Identify the preparation type.
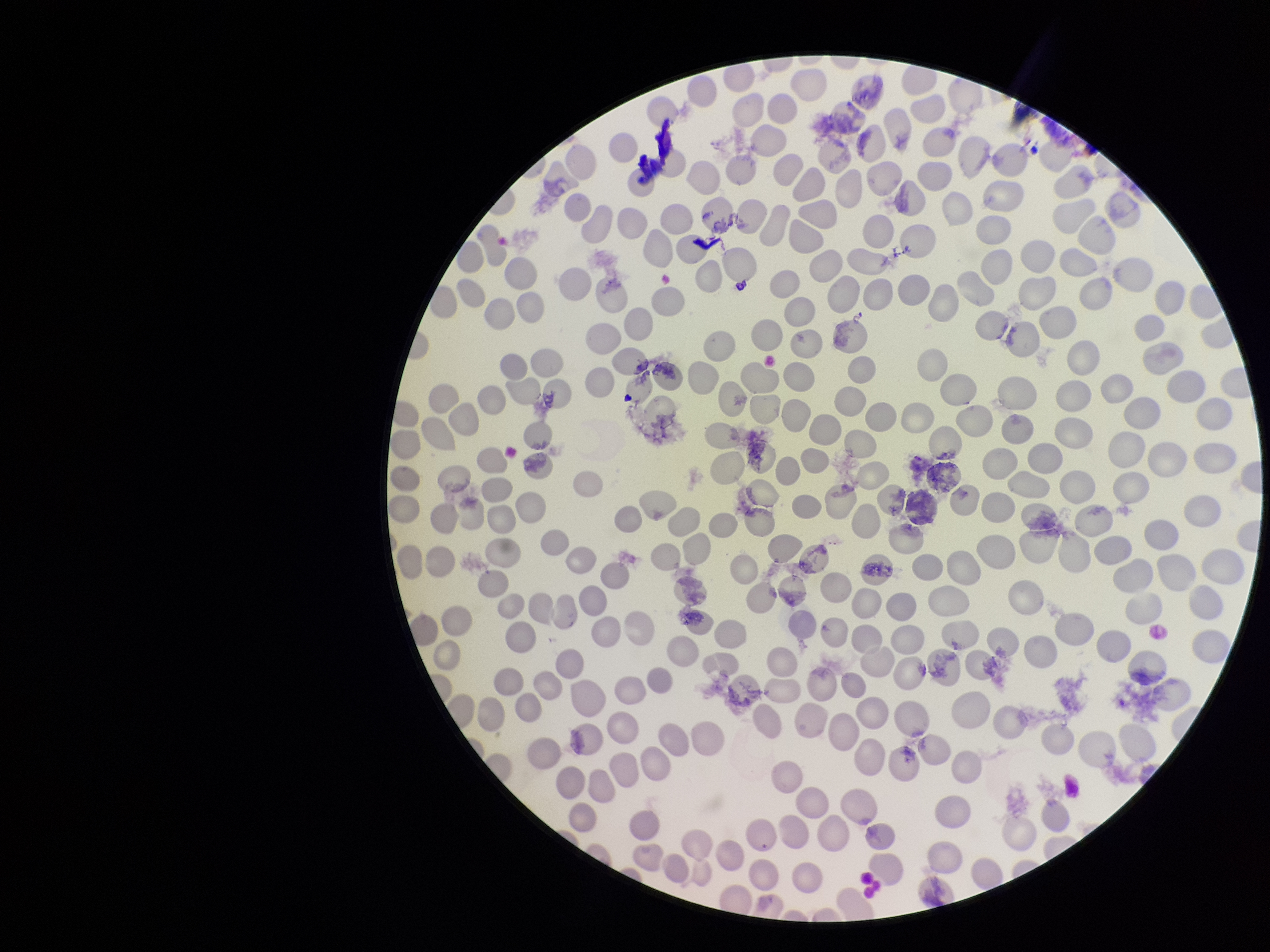

It is a thin blood smear.

Summary:
  - Parasitized red blood cell count: 0
  - Species reported for this patient: Plasmodium falciparum
  - Red blood cell count: 307
  - Stain: Giemsa
  - Field of view: one from this slide
  - Capture: smartphone photograph through the microscope eyepiece
  - Patient malaria status: infected
  - Parasitized red blood cells: none identified
  - Image size: 1270×952 pixels